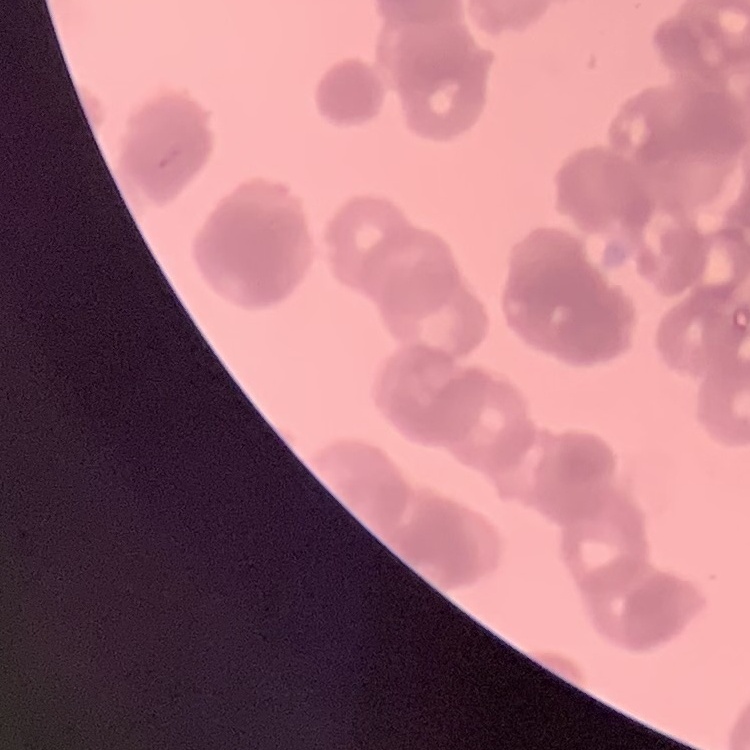

red blood cell morphology = rouleaux formation
stain = Field's or Giemsa
preparation = thin peripheral smear
image type = square crop of a larger photomicrograph